Give the extent of all uninfected red blood cells.
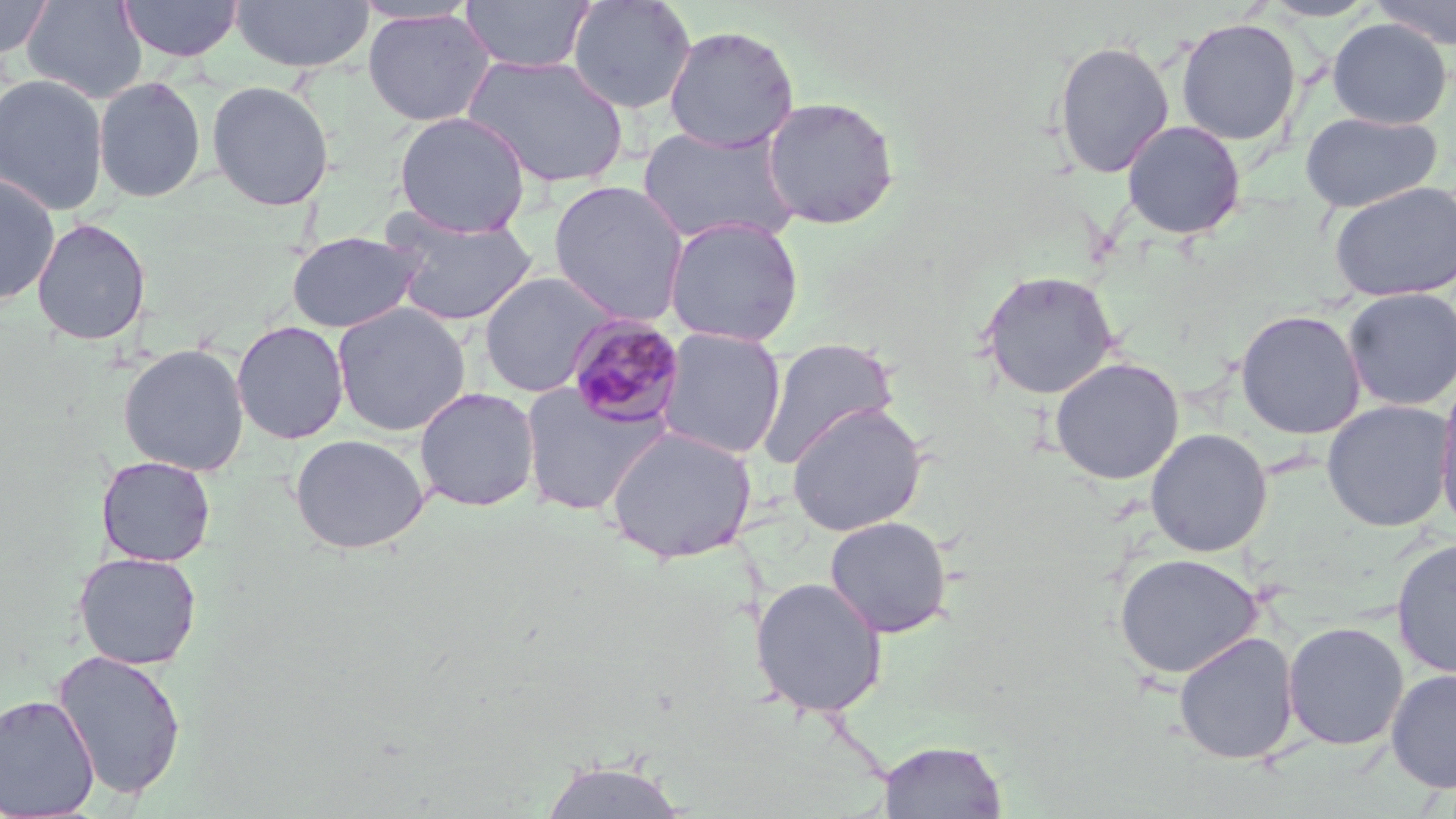
Approximate bounding boxes as (x1,y1)-(x2,y2) corner pairs in pixels.
Uninfected red blood cells: (0,0)-(54,60), (22,0)-(147,104), (117,0)-(243,62), (231,0)-(374,74), (460,0)-(595,74), (566,0)-(698,115), (1261,0)-(1379,22), (1370,1)-(1456,49), (362,8)-(496,127), (1174,17)-(1302,146), (1327,18)-(1452,129), (663,24)-(799,152), (1052,39)-(1175,179), (463,54)-(630,188), (0,73)-(109,216), (93,76)-(207,203), (206,80)-(334,211), (761,95)-(900,230), (393,111)-(531,238), (1299,111)-(1442,213), (1121,119)-(1246,240), (638,124)-(801,247), (0,171)-(60,306), (548,180)-(690,326), (1327,181)-(1456,302), (380,207)-(539,326), (663,215)-(804,347), (31,217)-(151,346), (286,230)-(424,333), (477,270)-(620,397), (979,270)-(1120,400), (1342,287)-(1456,411), (331,302)-(471,437), (1235,309)-(1365,439), (231,320)-(349,444), (657,327)-(786,460), (756,337)-(899,469), (118,343)-(249,477), (1049,357)-(1184,485), (1434,374)-(1456,537), (520,383)-(669,517), (413,386)-(540,512), (1321,399)-(1455,532), (786,402)-(928,536), (605,425)-(758,565), (1145,428)-(1273,557), (290,433)-(430,554), (96,454)-(216,567), (824,515)-(953,638), (1391,537)-(1456,679), (74,551)-(202,670), (1113,553)-(1264,679), (749,576)-(888,718), (1283,621)-(1409,750), (1173,631)-(1299,765), (52,647)-(187,800), (1386,668)-(1456,794), (1,694)-(99,817), (877,739)-(1008,818), (537,756)-(693,819).

Plasmodium malariae-infected red blood cell locations: (564,314)-(687,430). Slide-level diagnosis: Plasmodium malariae. Single field of view. Light microscopy. 1000x magnification. Image is 1456×819 pixels. Thin blood film. May-Grünwald-Giemsa-stained preparation.